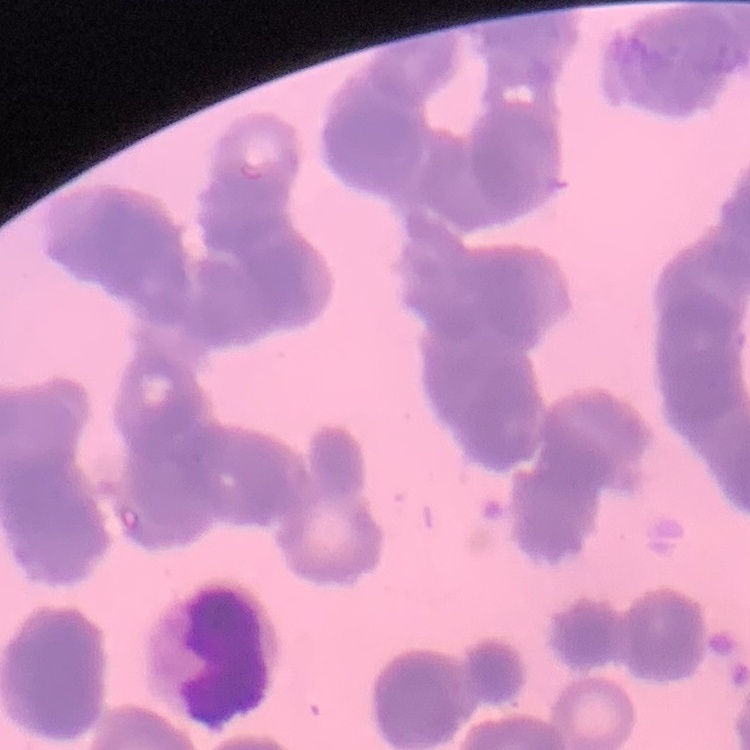

Summary:
  - Red blood cell morphology: rouleaux formation
  - Stain: Field's or Giemsa
  - Image type: one tile cut from a larger photomicrograph
  - Preparation: thin blood smear